Point out each Plasmodium parasite and each leukocyte.
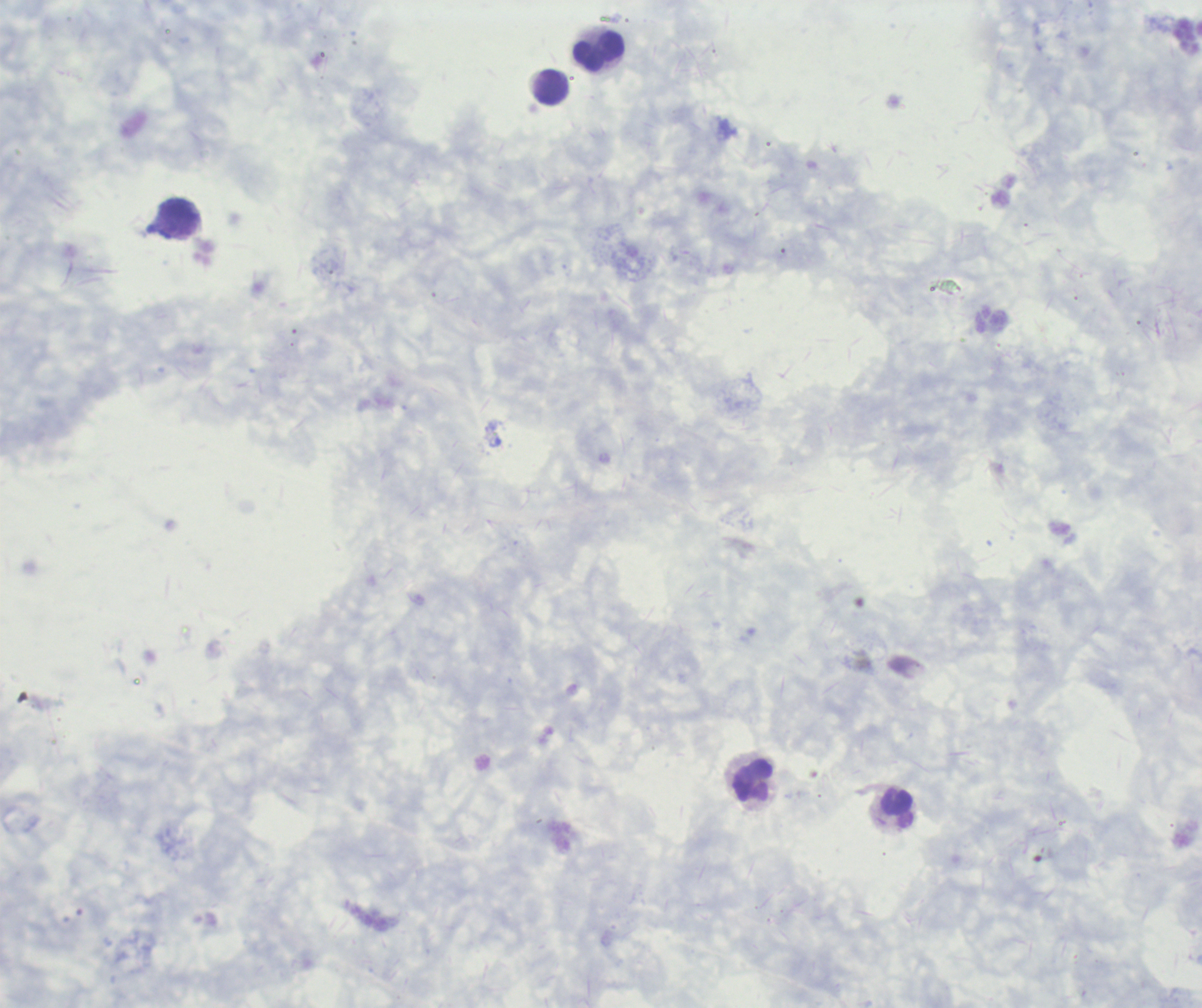

Negative for Plasmodium parasites.
Approximate centers as (x, y) in pixels.
Leukocytes: (599, 52), (552, 87), (180, 212), (754, 781), (899, 809).

{
  "context": "previously used in a real diagnosis",
  "preparation": "thick smear of blood",
  "coloration_quality": "good",
  "magnification": "100x",
  "image_size": "1202×1008 pixels",
  "background_quality": "poor",
  "field_of_view": "single",
  "stain": "Romanowsky"
}